Assess the morphology of the red blood cells.
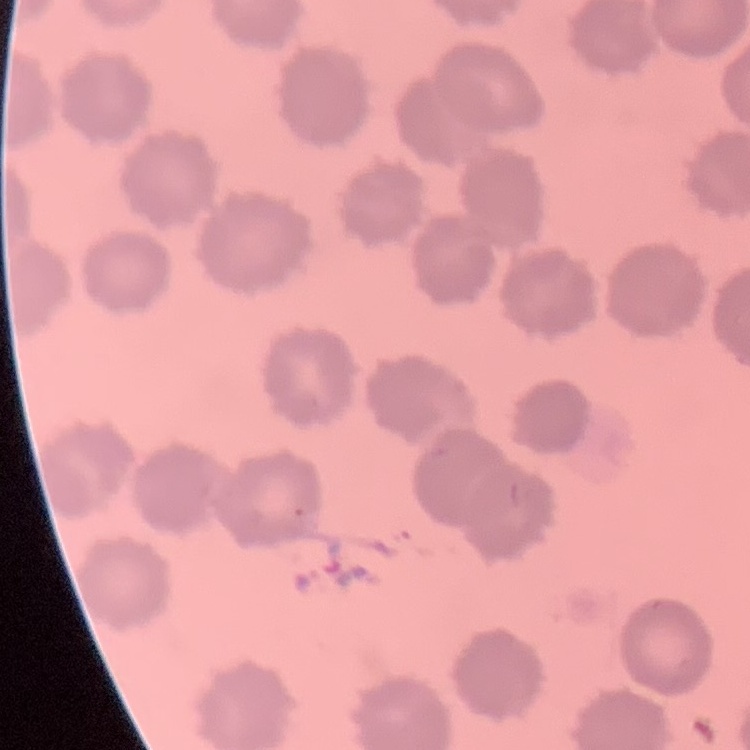

They show no rouleaux formation.

Summary:
  - Image type: one tile cut from a larger photomicrograph
  - Stain: Field's or Giemsa
  - Preparation: thin blood film